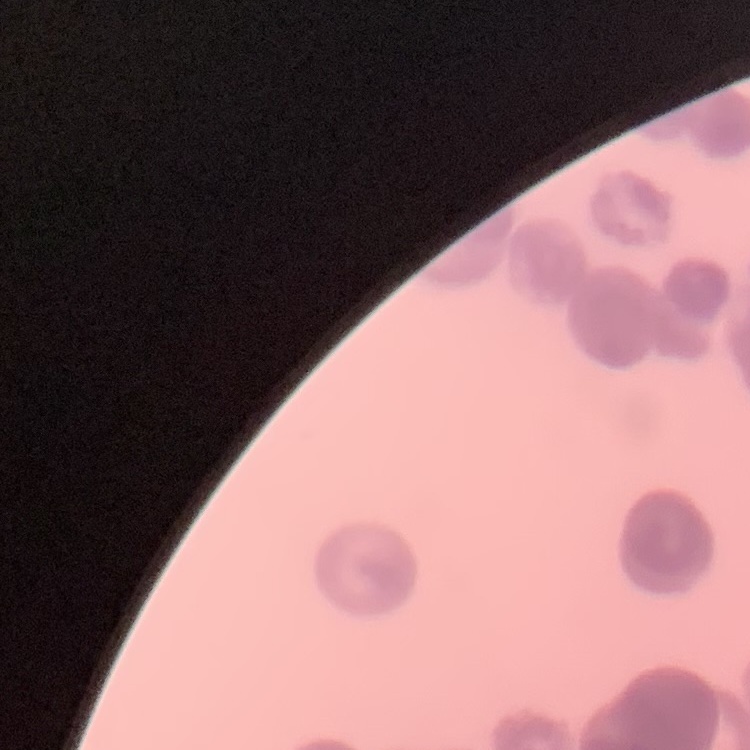
Summary:
  - Erythrocyte morphology: rouleaux formation
  - Stain: Field's or Giemsa
  - Image type: square crop of a larger photomicrograph
  - Preparation: thin peripheral smear